Identify the blood parasite species.
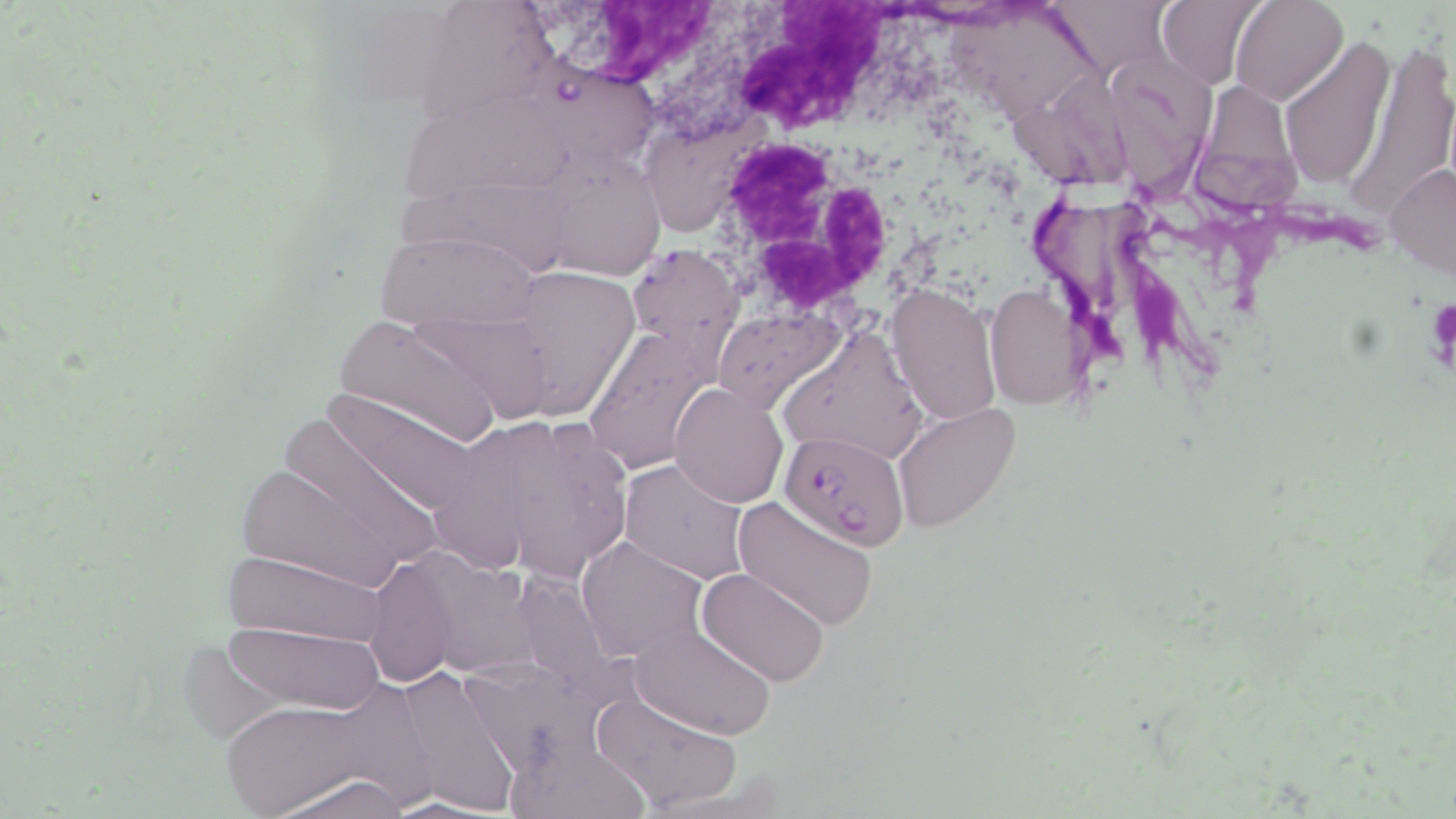
Plasmodium falciparum.

Summary:
  - Coordinate format: approximate bounding boxes as [x1, y1, x2, y2] in pixels
  - Plasmodium falciparum-infected red blood cell locations: [780, 430, 908, 550]
  - Uninfected red blood cell locations: [1157, 0, 1268, 89], [1229, 0, 1347, 106], [582, 1, 936, 150], [1047, 1, 1175, 82], [418, 2, 564, 131], [930, 7, 1090, 123], [1341, 33, 1456, 219], [1280, 39, 1396, 190], [538, 59, 669, 164], [1119, 67, 1220, 220], [1028, 72, 1136, 197], [1201, 86, 1307, 228], [416, 104, 589, 188], [643, 121, 763, 229], [571, 151, 654, 290], [1385, 161, 1456, 281], [393, 174, 576, 277], [369, 232, 534, 333], [627, 243, 744, 369], [535, 256, 647, 433], [886, 283, 1002, 427], [984, 287, 1083, 409], [413, 305, 558, 424], [714, 309, 838, 415], [783, 311, 937, 456], [334, 315, 495, 444], [582, 327, 710, 472], [327, 375, 497, 499], [670, 381, 790, 509], [893, 402, 1020, 534], [493, 406, 610, 590], [283, 412, 454, 568], [426, 422, 539, 586], [229, 457, 413, 589], [619, 460, 749, 586], [730, 493, 881, 632], [577, 538, 706, 662], [221, 550, 390, 644], [365, 551, 453, 684], [420, 556, 559, 686], [697, 566, 829, 688], [513, 575, 638, 702], [215, 622, 393, 712], [631, 625, 773, 738], [394, 660, 531, 818], [591, 690, 740, 813], [217, 695, 409, 815], [508, 735, 654, 818], [271, 772, 414, 818]
  - Platelet locations: [1427, 296, 1455, 378]
  - White blood cell locations: [725, 150, 914, 319]
  - Field of view: one of a larger specimen
  - Magnification: 1000x
  - Modality: light microscopy
  - Image size: 1456×819 pixels
  - Stain: May-Grünwald-Giemsa
  - Preparation: thin blood smear